Locate and identify every blood parasite.
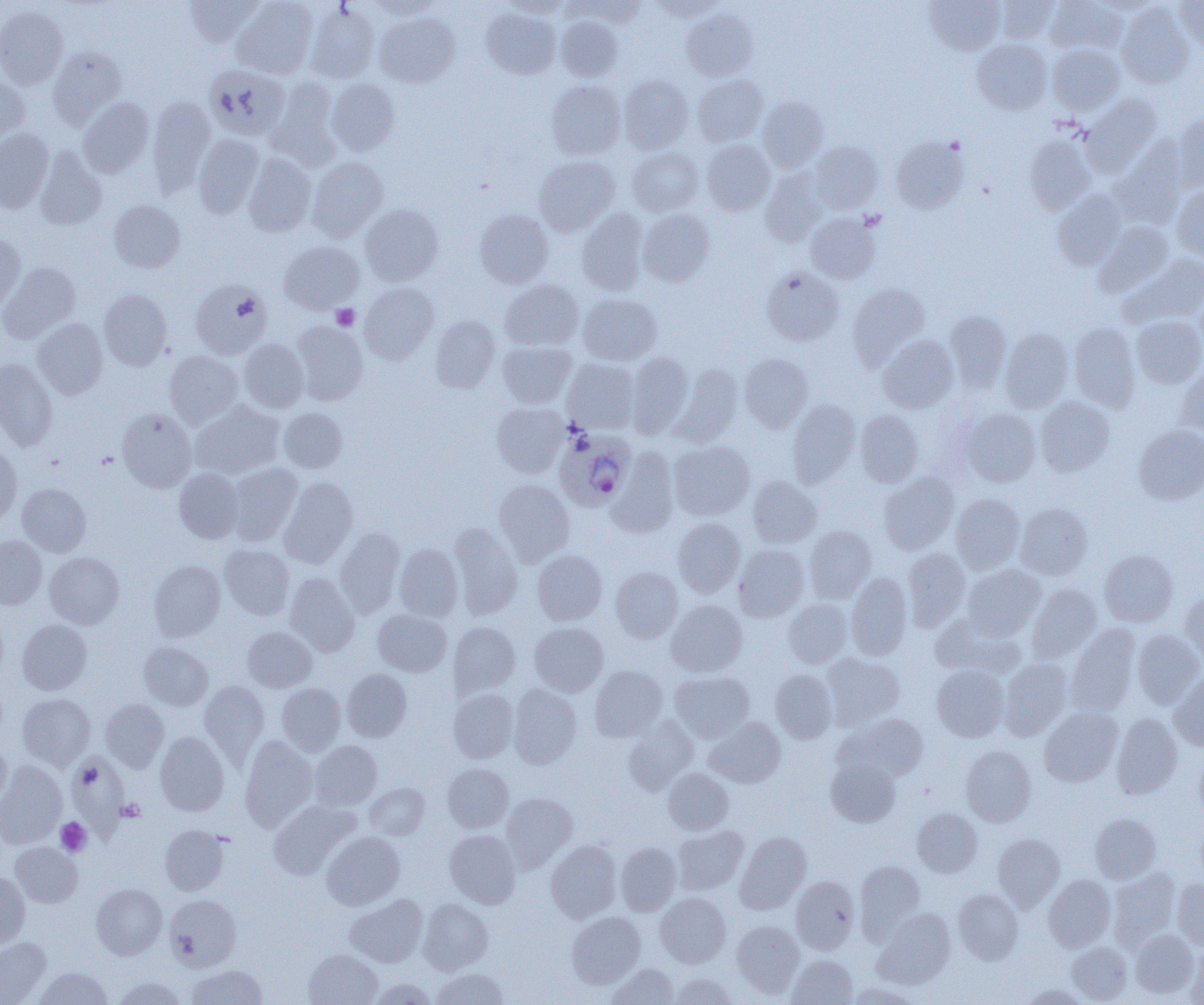
Approximate bounding boxes as named x1/y1/x2/y2 corners in pixels.
Plasmodium ovale-infected red blood cells: (x1=555, y1=429, x2=636, y2=510).
No Plasmodium falciparum, Plasmodium malariae, Plasmodium vivax, Babesia divergens, or Trypanosoma brucei observed.

Uninfected red blood cell locations: (x1=183, y1=0, x2=264, y2=47), (x1=368, y1=0, x2=445, y2=20), (x1=502, y1=0, x2=574, y2=18), (x1=648, y1=0, x2=727, y2=20), (x1=924, y1=0, x2=1005, y2=55), (x1=995, y1=0, x2=1058, y2=43), (x1=1045, y1=0, x2=1127, y2=54), (x1=1174, y1=0, x2=1204, y2=52), (x1=231, y1=1, x2=318, y2=79), (x1=573, y1=1, x2=648, y2=25), (x1=1117, y1=3, x2=1195, y2=88), (x1=0, y1=5, x2=68, y2=89), (x1=305, y1=5, x2=380, y2=83), (x1=481, y1=8, x2=560, y2=79), (x1=681, y1=9, x2=757, y2=81), (x1=375, y1=12, x2=460, y2=86), (x1=555, y1=16, x2=622, y2=81), (x1=971, y1=39, x2=1052, y2=115), (x1=1047, y1=44, x2=1124, y2=114), (x1=48, y1=47, x2=127, y2=126), (x1=204, y1=64, x2=290, y2=140), (x1=619, y1=74, x2=693, y2=153), (x1=693, y1=75, x2=768, y2=146), (x1=0, y1=77, x2=30, y2=144), (x1=269, y1=77, x2=340, y2=168), (x1=326, y1=78, x2=400, y2=155), (x1=546, y1=81, x2=626, y2=159), (x1=1081, y1=94, x2=1160, y2=175), (x1=147, y1=96, x2=216, y2=195), (x1=757, y1=96, x2=829, y2=172), (x1=77, y1=97, x2=154, y2=178), (x1=1174, y1=112, x2=1204, y2=191), (x1=0, y1=129, x2=53, y2=213), (x1=193, y1=134, x2=264, y2=217), (x1=1024, y1=135, x2=1095, y2=215), (x1=891, y1=136, x2=968, y2=213), (x1=701, y1=139, x2=775, y2=215), (x1=808, y1=140, x2=883, y2=213), (x1=1114, y1=143, x2=1188, y2=226), (x1=35, y1=146, x2=107, y2=230), (x1=627, y1=147, x2=703, y2=216), (x1=243, y1=153, x2=316, y2=236), (x1=534, y1=155, x2=620, y2=236), (x1=307, y1=156, x2=388, y2=242), (x1=760, y1=169, x2=829, y2=247), (x1=1172, y1=185, x2=1204, y2=261), (x1=1053, y1=191, x2=1127, y2=269), (x1=109, y1=200, x2=185, y2=273), (x1=359, y1=204, x2=443, y2=285), (x1=576, y1=208, x2=648, y2=295), (x1=638, y1=209, x2=715, y2=286), (x1=475, y1=210, x2=553, y2=288), (x1=806, y1=212, x2=880, y2=284), (x1=1094, y1=222, x2=1173, y2=297), (x1=0, y1=234, x2=26, y2=313), (x1=279, y1=241, x2=363, y2=313), (x1=1120, y1=254, x2=1204, y2=327), (x1=0, y1=263, x2=80, y2=343), (x1=761, y1=268, x2=844, y2=346), (x1=190, y1=279, x2=272, y2=360), (x1=501, y1=280, x2=584, y2=350), (x1=359, y1=283, x2=439, y2=363), (x1=847, y1=283, x2=930, y2=370), (x1=98, y1=289, x2=172, y2=370), (x1=577, y1=293, x2=661, y2=365), (x1=944, y1=310, x2=1012, y2=391), (x1=1132, y1=315, x2=1204, y2=388), (x1=430, y1=316, x2=500, y2=393), (x1=33, y1=318, x2=108, y2=399), (x1=292, y1=321, x2=369, y2=405), (x1=1069, y1=323, x2=1140, y2=412), (x1=1000, y1=328, x2=1074, y2=412), (x1=877, y1=335, x2=959, y2=413), (x1=239, y1=338, x2=309, y2=412), (x1=498, y1=341, x2=575, y2=408), (x1=164, y1=351, x2=243, y2=428), (x1=626, y1=352, x2=694, y2=437), (x1=739, y1=353, x2=814, y2=432), (x1=562, y1=358, x2=640, y2=434), (x1=0, y1=359, x2=58, y2=451), (x1=670, y1=363, x2=743, y2=446), (x1=1178, y1=364, x2=1204, y2=438), (x1=1034, y1=396, x2=1114, y2=476), (x1=787, y1=399, x2=860, y2=486), (x1=190, y1=400, x2=285, y2=480), (x1=491, y1=402, x2=567, y2=478), (x1=279, y1=407, x2=348, y2=473), (x1=116, y1=408, x2=196, y2=492), (x1=960, y1=408, x2=1040, y2=487), (x1=855, y1=410, x2=923, y2=487), (x1=1133, y1=425, x2=1204, y2=504), (x1=669, y1=441, x2=755, y2=520), (x1=0, y1=445, x2=22, y2=528), (x1=607, y1=448, x2=679, y2=537), (x1=226, y1=463, x2=303, y2=545), (x1=174, y1=468, x2=244, y2=543), (x1=878, y1=472, x2=959, y2=554), (x1=747, y1=476, x2=822, y2=548), (x1=278, y1=477, x2=358, y2=567), (x1=494, y1=479, x2=574, y2=566), (x1=17, y1=483, x2=91, y2=556), (x1=951, y1=494, x2=1025, y2=573), (x1=1016, y1=503, x2=1092, y2=579), (x1=673, y1=518, x2=745, y2=597), (x1=449, y1=523, x2=522, y2=620), (x1=804, y1=525, x2=876, y2=602), (x1=335, y1=527, x2=405, y2=617), (x1=0, y1=536, x2=47, y2=609), (x1=220, y1=544, x2=294, y2=620), (x1=394, y1=544, x2=463, y2=621), (x1=734, y1=544, x2=809, y2=621), (x1=903, y1=548, x2=969, y2=630), (x1=1099, y1=549, x2=1178, y2=627), (x1=533, y1=550, x2=607, y2=626), (x1=44, y1=552, x2=124, y2=629), (x1=149, y1=560, x2=226, y2=641), (x1=963, y1=564, x2=1046, y2=639), (x1=611, y1=567, x2=682, y2=642), (x1=846, y1=572, x2=912, y2=660), (x1=284, y1=573, x2=360, y2=657), (x1=1027, y1=584, x2=1101, y2=662), (x1=1180, y1=590, x2=1204, y2=663), (x1=783, y1=598, x2=852, y2=668), (x1=667, y1=600, x2=747, y2=676), (x1=0, y1=607, x2=9, y2=687), (x1=373, y1=609, x2=451, y2=677), (x1=931, y1=612, x2=1024, y2=680), (x1=17, y1=619, x2=92, y2=694), (x1=448, y1=622, x2=520, y2=698), (x1=529, y1=622, x2=608, y2=697), (x1=1067, y1=624, x2=1141, y2=716), (x1=243, y1=627, x2=317, y2=692), (x1=1132, y1=629, x2=1203, y2=708), (x1=139, y1=641, x2=213, y2=710), (x1=821, y1=653, x2=905, y2=730), (x1=999, y1=658, x2=1072, y2=740), (x1=590, y1=665, x2=667, y2=742), (x1=932, y1=665, x2=1010, y2=741), (x1=341, y1=668, x2=412, y2=742), (x1=770, y1=668, x2=837, y2=744), (x1=670, y1=670, x2=754, y2=742), (x1=1170, y1=673, x2=1204, y2=751), (x1=199, y1=680, x2=269, y2=764), (x1=277, y1=682, x2=345, y2=755), (x1=508, y1=684, x2=582, y2=768), (x1=449, y1=689, x2=518, y2=763), (x1=17, y1=693, x2=95, y2=769), (x1=100, y1=699, x2=169, y2=772), (x1=1039, y1=707, x2=1122, y2=786), (x1=1111, y1=713, x2=1182, y2=799), (x1=844, y1=714, x2=929, y2=781), (x1=623, y1=716, x2=699, y2=795), (x1=705, y1=717, x2=786, y2=788), (x1=154, y1=731, x2=229, y2=816), (x1=239, y1=736, x2=318, y2=832), (x1=310, y1=740, x2=382, y2=810), (x1=0, y1=741, x2=11, y2=810), (x1=961, y1=745, x2=1037, y2=827), (x1=1194, y1=751, x2=1204, y2=822), (x1=66, y1=752, x2=129, y2=842), (x1=825, y1=755, x2=902, y2=828), (x1=0, y1=761, x2=67, y2=849), (x1=443, y1=764, x2=514, y2=832), (x1=663, y1=768, x2=734, y2=835), (x1=365, y1=783, x2=429, y2=839), (x1=501, y1=792, x2=577, y2=872), (x1=268, y1=800, x2=357, y2=879), (x1=912, y1=808, x2=982, y2=877), (x1=1090, y1=813, x2=1161, y2=883), (x1=1195, y1=817, x2=1204, y2=887), (x1=159, y1=825, x2=229, y2=895), (x1=673, y1=825, x2=749, y2=894), (x1=445, y1=830, x2=520, y2=908), (x1=322, y1=831, x2=405, y2=910), (x1=735, y1=832, x2=811, y2=914), (x1=993, y1=833, x2=1064, y2=911), (x1=545, y1=840, x2=621, y2=923), (x1=10, y1=842, x2=83, y2=907), (x1=615, y1=843, x2=681, y2=915), (x1=855, y1=859, x2=925, y2=939), (x1=1110, y1=868, x2=1180, y2=946), (x1=0, y1=871, x2=30, y2=949), (x1=1044, y1=874, x2=1115, y2=951), (x1=791, y1=875, x2=859, y2=954), (x1=1172, y1=879, x2=1204, y2=948), (x1=91, y1=884, x2=167, y2=959), (x1=953, y1=889, x2=1023, y2=964), (x1=656, y1=893, x2=730, y2=967), (x1=165, y1=894, x2=242, y2=971), (x1=346, y1=894, x2=427, y2=968), (x1=418, y1=898, x2=493, y2=974), (x1=872, y1=909, x2=956, y2=988), (x1=567, y1=912, x2=645, y2=988), (x1=732, y1=920, x2=804, y2=997), (x1=1131, y1=929, x2=1198, y2=998), (x1=0, y1=937, x2=51, y2=1004), (x1=1066, y1=942, x2=1132, y2=1003), (x1=1185, y1=947, x2=1204, y2=1004), (x1=304, y1=949, x2=382, y2=1005), (x1=787, y1=955, x2=857, y2=1004), (x1=606, y1=963, x2=680, y2=1004), (x1=186, y1=965, x2=267, y2=1005), (x1=34, y1=967, x2=112, y2=1005), (x1=431, y1=968, x2=508, y2=1005), (x1=669, y1=974, x2=737, y2=1004), (x1=111, y1=977, x2=188, y2=1005), (x1=369, y1=978, x2=438, y2=1005), (x1=847, y1=982, x2=919, y2=1005), (x1=1020, y1=984, x2=1088, y2=1005). Platelet locations: (x1=331, y1=305, x2=360, y2=331), (x1=117, y1=799, x2=145, y2=822), (x1=55, y1=817, x2=92, y2=857). Slide-level diagnosis: Plasmodium ovale. Optical microscopy. Thin blood film. Image is 1204×1005 pixels. Captured at 1000x magnification. One field of a larger specimen.